Name the blood parasite species.
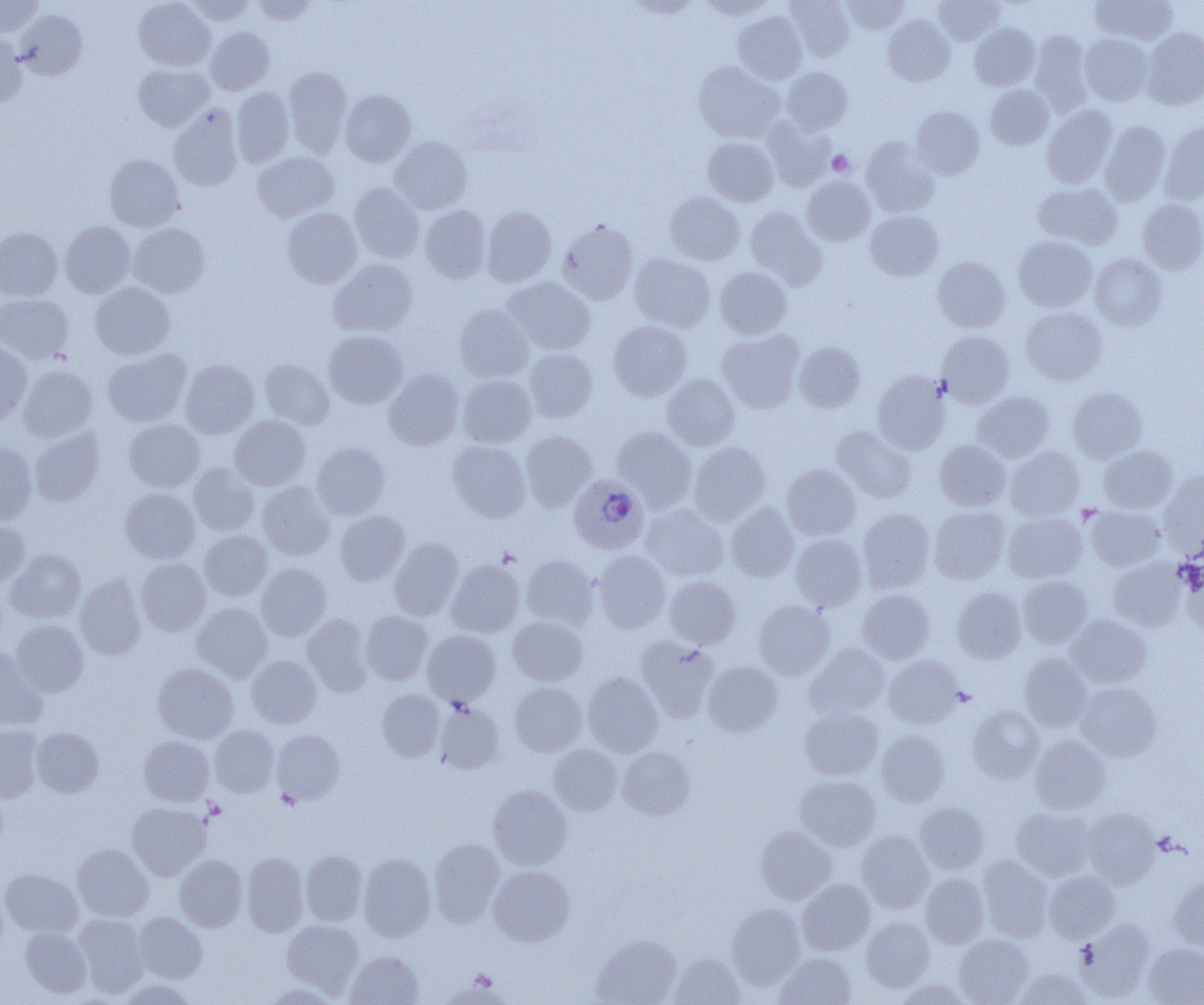

Plasmodium ovale.

Approximate bounding boxes as [x1, y1, x2, y2] in pixels. Uninfected red blood cell locations: [0, 0, 44, 36], [133, 0, 215, 71], [184, 0, 255, 25], [252, 0, 319, 24], [625, 0, 703, 18], [698, 0, 777, 19], [786, 0, 855, 61], [841, 0, 910, 34], [932, 0, 1005, 46], [1091, 0, 1177, 45], [14, 9, 87, 79], [733, 11, 807, 84], [883, 15, 955, 86], [969, 23, 1040, 90], [206, 27, 274, 94], [1141, 28, 1204, 109], [0, 31, 26, 108], [1029, 31, 1093, 115], [1080, 33, 1153, 106], [694, 62, 784, 143], [133, 64, 214, 131], [283, 66, 351, 157], [782, 67, 852, 134], [985, 85, 1053, 149], [232, 87, 294, 167], [339, 90, 416, 167], [1042, 104, 1117, 188], [168, 105, 243, 191], [911, 105, 984, 179], [762, 120, 835, 192], [1100, 121, 1171, 205], [1159, 121, 1204, 204], [389, 136, 472, 214], [703, 137, 778, 206], [862, 138, 940, 217], [253, 151, 339, 221], [104, 153, 184, 232], [802, 177, 875, 245], [1034, 182, 1122, 248], [349, 183, 424, 263], [665, 192, 745, 265], [1138, 199, 1204, 274], [419, 205, 490, 283], [481, 206, 556, 286], [282, 208, 362, 288], [746, 208, 825, 286], [865, 210, 943, 280], [558, 219, 638, 305], [60, 221, 135, 298], [128, 223, 209, 297], [0, 227, 62, 301], [1013, 236, 1097, 311], [630, 253, 715, 332], [1090, 254, 1167, 330], [933, 257, 1010, 332], [329, 259, 418, 336], [715, 267, 791, 338], [504, 277, 595, 354], [90, 282, 175, 359], [0, 293, 74, 364], [454, 305, 533, 382], [1020, 306, 1107, 385], [609, 321, 691, 400], [717, 329, 804, 412], [324, 330, 408, 408], [938, 331, 1014, 407], [0, 339, 32, 424], [793, 341, 866, 412], [103, 348, 191, 427], [525, 349, 597, 423], [180, 359, 259, 438], [260, 359, 334, 429], [18, 365, 97, 441], [385, 370, 463, 450], [873, 371, 950, 454], [662, 374, 740, 449], [458, 375, 536, 447], [1068, 387, 1146, 462], [974, 390, 1054, 461], [230, 415, 310, 490], [124, 419, 205, 492], [832, 426, 915, 503], [30, 427, 105, 506], [613, 427, 696, 509], [521, 430, 596, 511], [934, 439, 1010, 510], [447, 440, 531, 522], [0, 441, 37, 523], [312, 442, 389, 518], [690, 442, 770, 524], [1099, 445, 1177, 513], [1006, 447, 1083, 519], [188, 464, 259, 536], [781, 464, 860, 540], [1159, 470, 1204, 553], [258, 482, 334, 560], [120, 488, 200, 563], [726, 503, 799, 581], [641, 504, 727, 580], [929, 506, 1009, 584], [1085, 506, 1165, 571], [857, 508, 935, 592], [335, 510, 409, 585], [1003, 512, 1087, 583], [0, 520, 30, 587], [199, 530, 272, 601], [790, 534, 866, 611], [389, 538, 462, 619], [5, 549, 85, 623], [595, 551, 670, 633], [521, 555, 599, 629], [136, 558, 211, 635], [447, 559, 525, 637], [1108, 559, 1186, 631], [256, 563, 331, 640], [75, 574, 146, 660], [664, 575, 741, 648], [1018, 576, 1093, 648], [952, 587, 1026, 663], [858, 589, 934, 664], [754, 601, 834, 679], [191, 602, 272, 682], [361, 611, 432, 685], [303, 614, 373, 695], [1066, 614, 1152, 689], [508, 616, 588, 685], [11, 620, 88, 697], [422, 630, 500, 705], [636, 635, 718, 722], [805, 643, 889, 719], [0, 646, 47, 730], [1019, 653, 1091, 731], [246, 655, 321, 728], [883, 655, 962, 728], [703, 661, 783, 736], [153, 663, 238, 743], [583, 672, 663, 756], [509, 681, 586, 756], [1076, 682, 1161, 761], [377, 688, 444, 761], [434, 702, 505, 774], [967, 705, 1043, 783], [800, 708, 883, 780], [0, 725, 44, 802], [210, 725, 279, 796], [31, 727, 104, 797], [272, 729, 345, 804], [876, 730, 950, 807], [139, 735, 214, 806], [1030, 735, 1110, 814], [548, 744, 623, 815], [617, 746, 695, 820], [796, 775, 881, 850], [488, 784, 572, 869], [127, 802, 211, 880], [915, 802, 989, 874], [1012, 806, 1096, 881], [1083, 808, 1159, 888], [755, 826, 836, 903], [856, 830, 934, 912], [428, 839, 505, 926], [72, 844, 153, 921], [301, 850, 367, 926], [241, 852, 309, 936], [359, 853, 435, 941], [174, 854, 247, 931], [978, 856, 1053, 942], [488, 865, 575, 945], [1, 869, 83, 937], [1044, 870, 1119, 942], [920, 873, 988, 948], [1169, 876, 1204, 950], [797, 878, 875, 955], [726, 903, 805, 988], [134, 912, 207, 983], [74, 914, 149, 996], [861, 917, 935, 991], [282, 919, 364, 995], [1076, 919, 1155, 1001], [21, 928, 92, 998], [591, 934, 681, 1005], [954, 934, 1033, 1004], [1143, 943, 1204, 1005], [345, 951, 424, 1005], [670, 953, 745, 1005], [775, 953, 856, 1005], [1014, 969, 1091, 1004], [117, 978, 195, 1005], [895, 979, 973, 1005], [262, 983, 340, 1004]. Plasmodium ovale-infected red blood cell locations: [569, 475, 649, 554]. Platelet locations: [827, 150, 854, 176], [1077, 504, 1102, 525], [498, 548, 521, 567], [952, 687, 976, 707], [277, 789, 301, 810], [203, 799, 225, 821], [469, 970, 497, 991]. Captured at 1000x magnification. One field of a larger specimen. Image is 1204×1005 pixels. Light microscopy. Thin blood smear.